Locate every Plasmodium parasite.
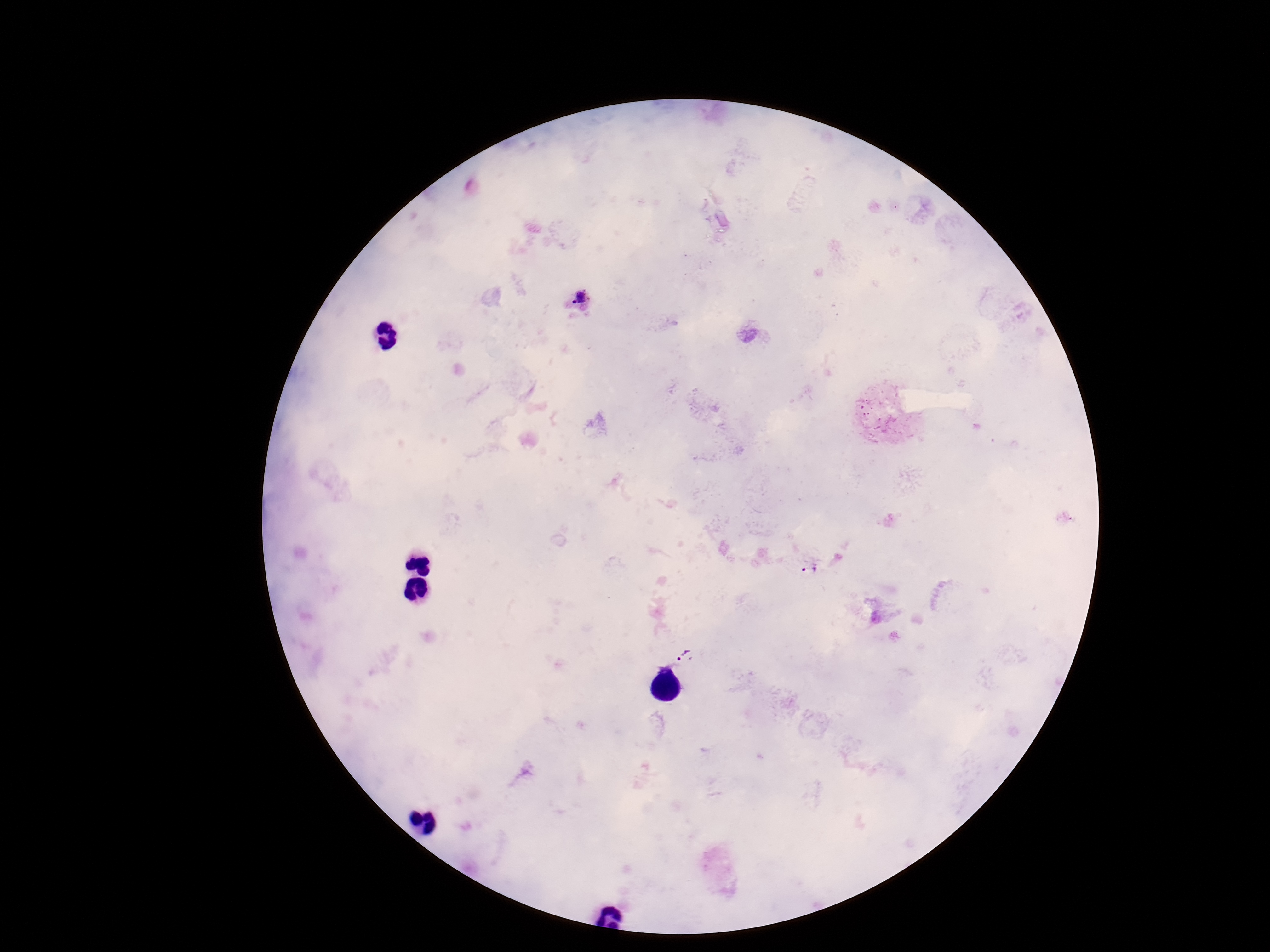
Approximate centers as [x, y] in pixels.
Plasmodium parasites: [579, 298], [809, 567], [685, 655].

Summary:
  - Stain: Giemsa
  - Patient malaria status: infected
  - Preparation: thick blood smear
  - Capture: smartphone camera through the microscope eyepiece
  - Magnification: 100x
  - Image size: 1270×952 pixels
  - Field of view: one from this slide